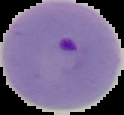
Summary:
  - Result: Plasmodium parasites identified
  - Image type: cell region segmented out of the field of view; surrounding area masked to black
  - Preparation: thin blood film
  - Image size: 124×115 pixels